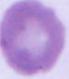
Summary:
  - Magnification: 1000x
  - Modality: micrograph
  - Identification: erythrocyte